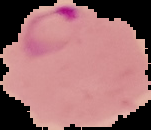
malaria status = parasitized
image type = cell region segmented out of the field of view; surrounding area masked to black
image size = 151×130 pixels
preparation = thin blood smear